Name the parasite shown.
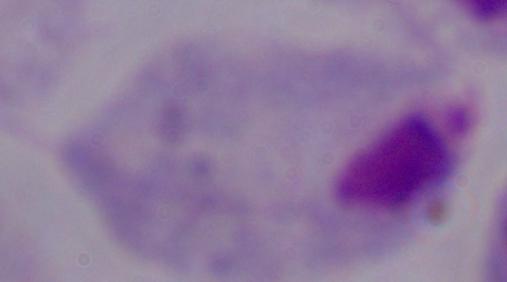
This is a trichomonad.

magnification: 1000x
modality: micrograph